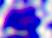
modality = micrograph
identification = leukocyte
magnification = 400x